Assess for parasitized red blood cells.
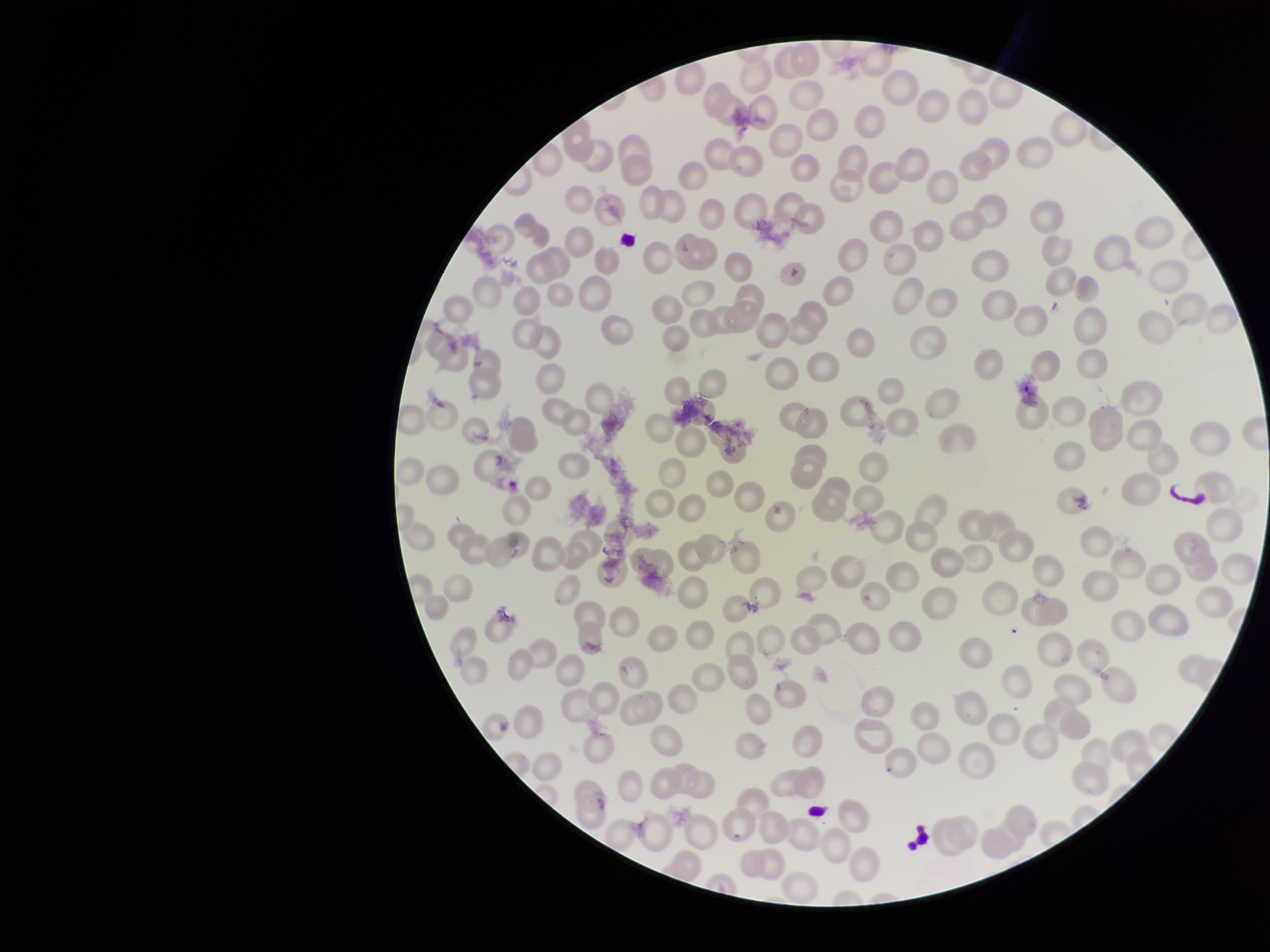

None seen.

Summary:
  - Stain: Giemsa
  - Capture: smartphone photograph through the microscope eyepiece
  - Red blood cell count: 209
  - Patient malaria status: positive
  - Parasitized red blood cell count: 0
  - Image size: 1270×952 pixels
  - Species reported for this patient: Plasmodium vivax
  - Field of view: one from this slide
  - Preparation: thin blood smear